Name the parasite shown.
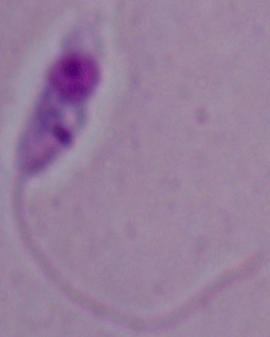

This is Leishmania.

modality: micrograph
magnification: 1000x